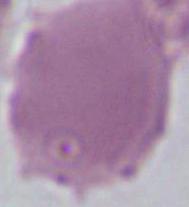

Summary:
  - Identification: red blood cell
  - Modality: photomicrograph
  - Magnification: 1000x